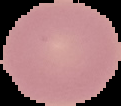 Result: negative for Plasmodium parasites. Image is 121×106 pixels. From a thin blood smear. Segmented cell region on a black background.